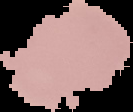
image size = 133×112 pixels
preparation = thin blood film
image type = cell region segmented out of the field of view; surrounding area masked to black
result = negative for Plasmodium parasites